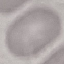

result = no malaria parasites seen
capture = smartphone through the microscope eyepiece
preparation = thin blood smear
stain = Giemsa
image type = cell patch, automatically extracted from a larger field of view and resized to 64 × 64 pixels